Name the parasite shown.
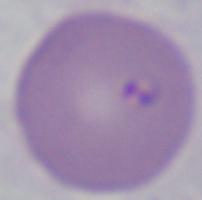

Babesia.

Summary:
  - Magnification: 1000x
  - Modality: photomicrograph